Classify this cell by malaria status.
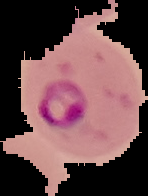
It is parasitized.

{
  "image_type": "cell region segmented out of the field of view; surrounding area masked to black",
  "preparation": "thin blood smear",
  "image_size": "148×196 pixels"
}